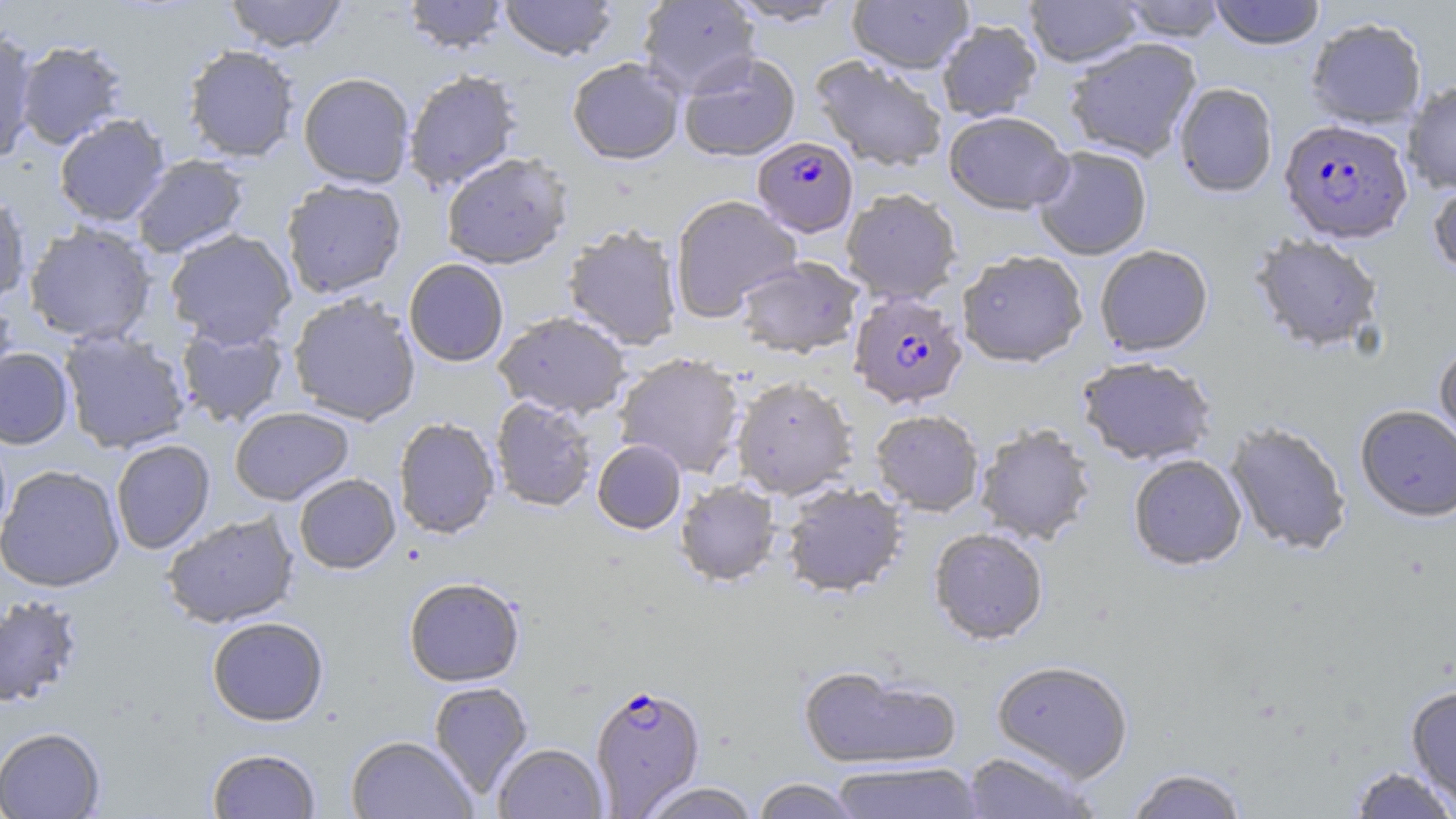

Summary:
  - Coordinate format: approximate bounding boxes as (x1, y1, x2, y2) in pixels
  - Uninfected red blood cell locations: (224, 0, 348, 52), (403, 0, 509, 54), (500, 0, 618, 61), (638, 0, 761, 97), (726, 0, 849, 26), (847, 0, 973, 74), (1025, 0, 1143, 67), (1119, 0, 1227, 42), (1209, 0, 1326, 50), (1306, 17, 1428, 129), (936, 20, 1042, 122), (0, 28, 38, 164), (1064, 38, 1202, 162), (15, 40, 128, 149), (182, 44, 300, 162), (679, 52, 801, 161), (811, 56, 948, 172), (567, 58, 685, 165), (403, 69, 522, 191), (298, 72, 415, 188), (1403, 81, 1456, 194), (1174, 82, 1278, 197), (943, 110, 1073, 215), (53, 113, 170, 227), (1032, 145, 1153, 260), (441, 152, 572, 269), (130, 154, 249, 258), (280, 178, 407, 298), (1428, 178, 1456, 280), (841, 188, 962, 304), (0, 189, 31, 305), (670, 194, 802, 322), (24, 222, 157, 345), (562, 224, 683, 350), (164, 228, 297, 348), (1249, 234, 1385, 355), (1094, 244, 1214, 357), (957, 250, 1088, 368), (734, 256, 864, 358), (404, 259, 509, 367), (0, 292, 18, 400), (287, 292, 421, 426), (494, 311, 632, 419), (175, 321, 290, 429), (58, 328, 192, 454), (1434, 340, 1456, 451), (0, 347, 74, 449), (613, 352, 746, 478), (1076, 356, 1217, 467), (731, 375, 858, 499), (490, 396, 598, 512), (1355, 404, 1456, 523), (229, 407, 353, 505), (870, 409, 985, 516), (393, 417, 500, 539), (1224, 420, 1352, 556), (974, 423, 1097, 546), (111, 439, 215, 554), (592, 439, 686, 534), (1128, 454, 1247, 570), (0, 464, 125, 592), (294, 473, 400, 574), (674, 480, 781, 586), (781, 482, 908, 598), (162, 511, 299, 629), (929, 528, 1049, 645), (403, 577, 525, 687), (0, 594, 85, 709), (207, 616, 329, 726), (992, 660, 1134, 781), (799, 664, 961, 771), (428, 681, 533, 799), (1406, 686, 1456, 809), (0, 726, 105, 818), (346, 735, 478, 819), (493, 743, 607, 819), (207, 748, 321, 819), (961, 751, 1098, 818), (830, 761, 983, 819), (1349, 766, 1455, 818), (1124, 767, 1250, 819), (751, 778, 863, 819), (639, 782, 761, 819)
  - Plasmodium falciparum-infected red blood cell locations: (1279, 118, 1412, 244), (752, 137, 858, 237), (848, 291, 968, 409), (589, 683, 706, 816)
  - Slide-level diagnosis: Plasmodium falciparum
  - Stain: May-Grünwald-Giemsa
  - Field of view: single
  - Modality: light microscopy
  - Image size: 1456×819 pixels
  - Magnification: 1000x
  - Preparation: thin blood film